Point out each leukocyte.
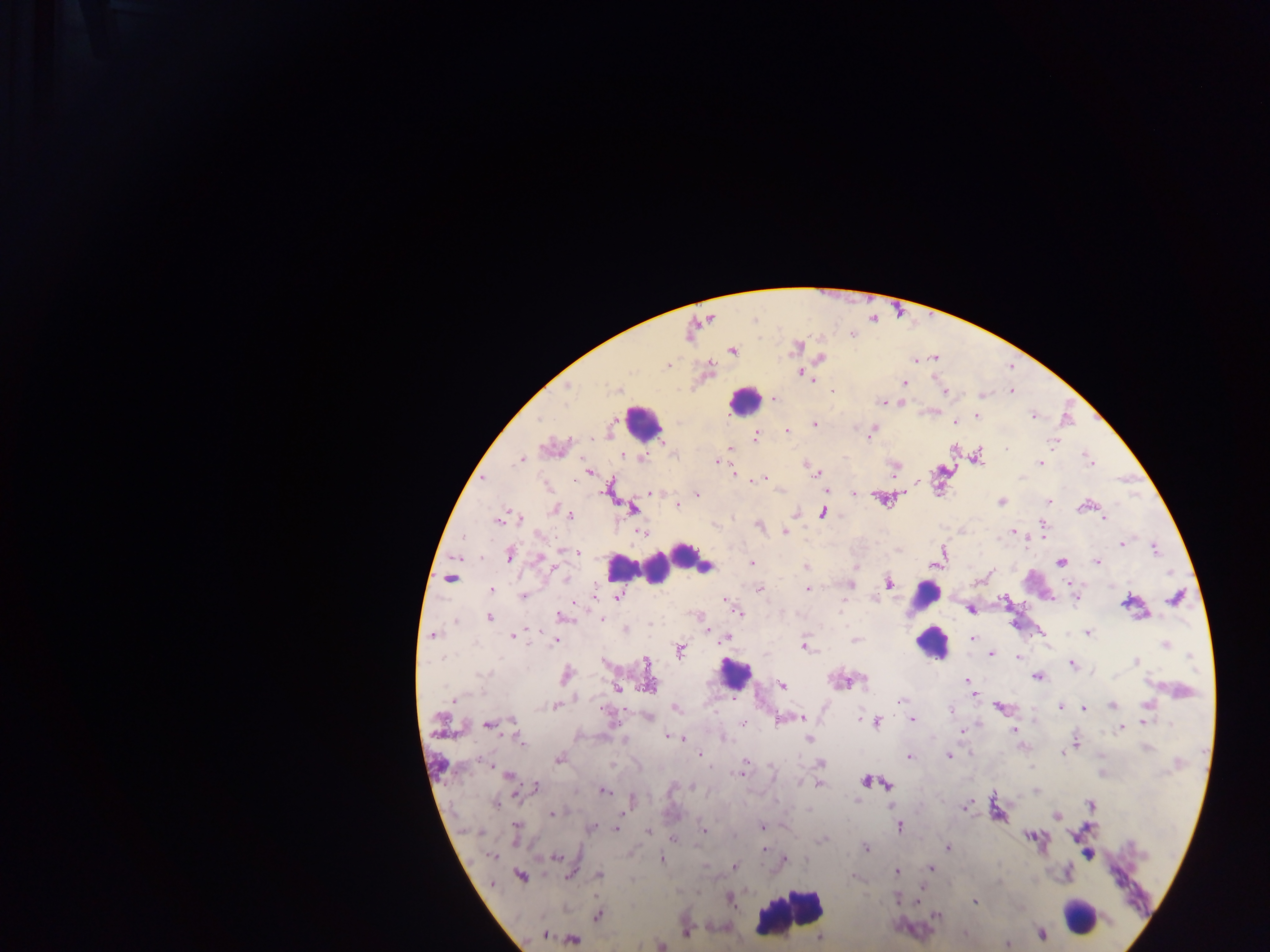

Approximate centers as {x, y} in pixels.
Leukocytes: {744, 400}, {643, 423}, {695, 558}, {621, 567}, {656, 568}, {925, 595}, {926, 623}, {931, 643}, {735, 674}, {790, 912}, {1081, 916}.

Plasmodium parasite locations: {733, 351}, {820, 357}, {668, 366}, {802, 374}, {905, 383}, {568, 388}, {617, 389}, {1011, 391}, {945, 392}, {981, 395}, {774, 399}, {882, 401}, {901, 402}, {977, 416}, {1033, 416}, {955, 421}, {815, 425}, {787, 431}, {872, 432}, {756, 436}, {1052, 442}, {729, 449}, {1007, 450}, {979, 455}, {1088, 458}, {642, 459}, {520, 460}, {718, 461}, {1041, 461}, {806, 465}, {894, 468}, {589, 473}, {733, 473}, {814, 473}, {763, 478}, {483, 480}, {548, 487}, {609, 490}, {652, 492}, {854, 493}, {697, 494}, {883, 499}, {1001, 501}, {1048, 501}, {682, 502}, {677, 505}, {1084, 506}, {632, 508}, {554, 510}, {823, 513}, {571, 515}, {520, 518}, {1104, 518}, {498, 520}, {759, 524}, {1044, 525}, {785, 531}, {641, 532}, {1014, 532}, {539, 535}, {1122, 543}, {1155, 549}, {568, 551}, {575, 553}, {510, 554}, {942, 555}, {542, 560}, {1060, 562}, {1097, 562}, {751, 563}, {936, 563}, {705, 567}, {805, 567}, {990, 573}, {565, 577}, {450, 578}, {889, 582}, {850, 586}, {759, 589}, {808, 589}, {492, 590}, {523, 595}, {618, 596}, {1174, 597}, {1075, 598}, {970, 609}, {735, 610}, {490, 617}, {562, 617}, {601, 619}, {455, 621}, {626, 629}, {1088, 633}, {433, 635}, {513, 636}, {724, 638}, {973, 638}, {556, 640}, {855, 640}, {1165, 645}, {805, 647}, {680, 652}, {991, 654}, {1018, 657}, {1136, 661}, {646, 663}, {1072, 664}, {482, 674}, {567, 675}, {1037, 677}, {967, 680}, {781, 685}, {649, 687}, {616, 688}, {973, 696}, {453, 700}, {901, 701}, {1112, 705}, {1147, 705}, {555, 706}, {998, 707}, {1061, 707}, {676, 708}, {1083, 708}, {951, 710}, {647, 717}, {801, 718}, {861, 719}, {912, 719}, {785, 720}, {513, 722}, {876, 722}, {1144, 722}, {743, 723}, {1171, 724}, {488, 725}, {1121, 728}, {1013, 731}, {962, 732}, {669, 736}, {681, 738}, {809, 738}, {520, 742}, {1076, 742}, {1146, 748}, {1062, 753}, {700, 755}, {949, 756}, {909, 757}, {559, 759}, {745, 762}, {821, 764}, {743, 768}, {740, 773}, {509, 776}, {866, 781}, {799, 782}, {819, 784}, {887, 785}, {535, 787}, {672, 788}, {692, 788}, {604, 791}, {1036, 791}, {857, 800}, {496, 803}, {1091, 805}, {965, 808}, {809, 810}, {553, 814}, {1057, 816}, {516, 827}, {762, 827}, {899, 827}, {592, 828}, {617, 829}, {703, 830}, {648, 831}, {1029, 836}, {674, 839}, {821, 841}, {865, 847}, {948, 848}, {764, 851}, {492, 856}, {557, 857}, {662, 859}, {785, 859}, {705, 866}, {734, 866}, {931, 868}, {897, 872}, {521, 875}, {599, 876}, {853, 877}, {999, 881}, {898, 898}, {730, 899}, {919, 902}, {975, 903}, {598, 915}, {936, 915}, {686, 934}, {1041, 934}, {965, 935}, {545, 936}, {820, 938}, {573, 939}, {1008, 944}, {661, 946}. Collected in Ghana. One field of view. Thick blood film. Image is 1270×952 pixels. Mobile-phone photograph taken through the microscope.